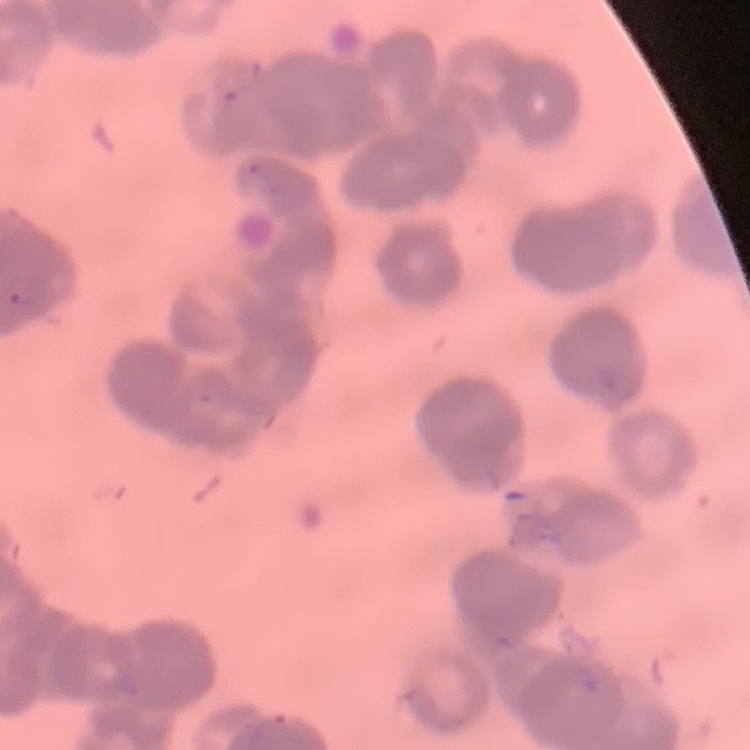
Summary:
  - Red blood cell morphology: rouleaux formation
  - Preparation: thin blood smear
  - Stain: Field's or Giemsa
  - Image type: square crop of a larger photomicrograph